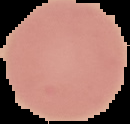
Summary:
  - Preparation: thin blood smear
  - Image size: 130×124 pixels
  - Image type: segmented cell region on a black background
  - Result: no malaria parasites seen